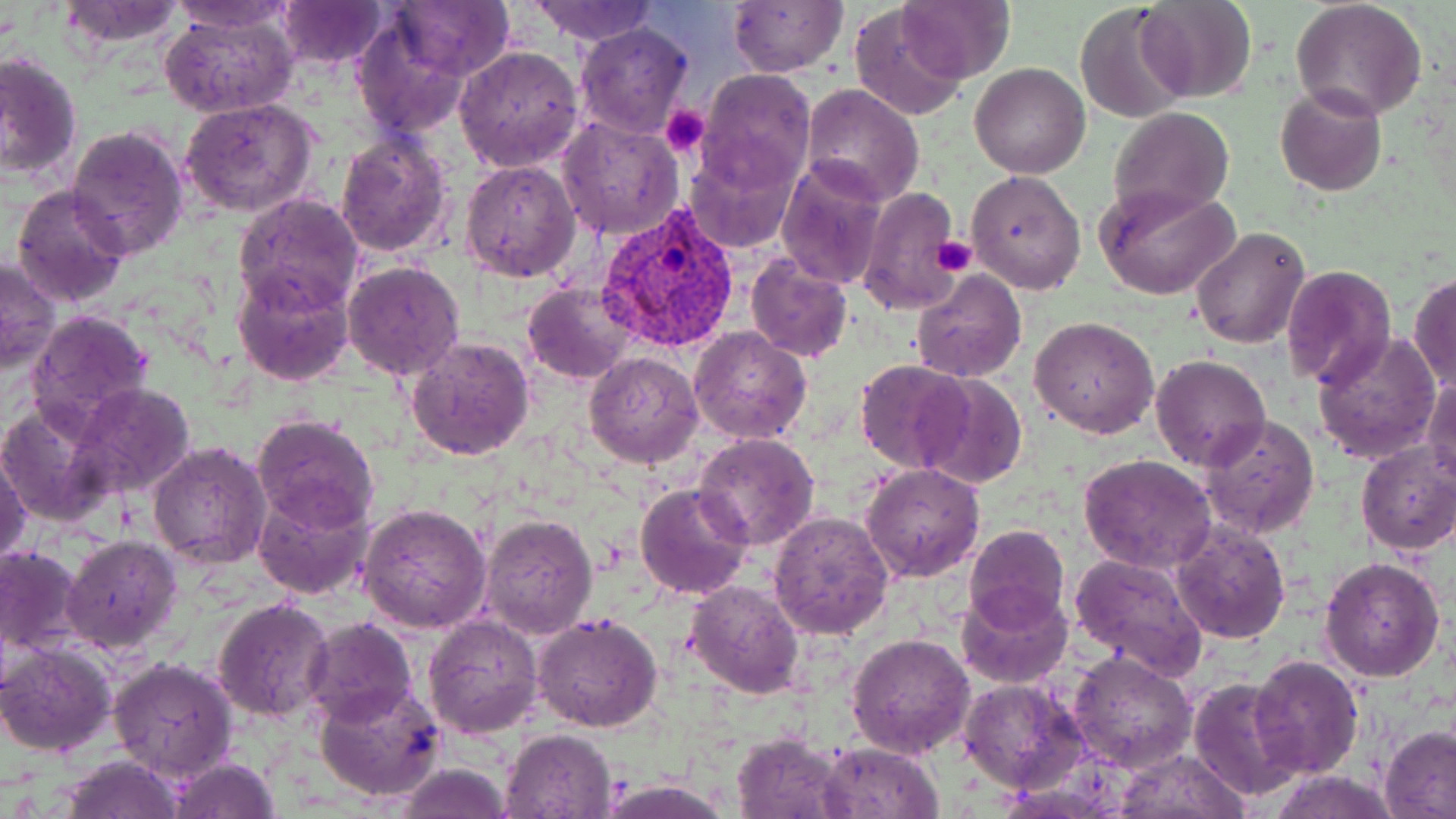

Approximate bounding boxes as (x1, y1, x2, y2) in pixels. Plasmodium vivax-infected red blood cell locations: (598, 202, 738, 356). Uninfected red blood cell locations: (171, 0, 297, 33), (277, 0, 388, 70), (285, 0, 509, 95), (390, 0, 512, 79), (899, 0, 1016, 83), (1135, 0, 1257, 102), (1291, 0, 1427, 120), (55, 1, 189, 50), (528, 1, 661, 47), (727, 1, 848, 76), (1073, 2, 1192, 123), (850, 8, 965, 122), (159, 10, 297, 117), (351, 14, 472, 137), (574, 23, 692, 138), (455, 45, 585, 172), (0, 51, 81, 180), (969, 63, 1091, 180), (696, 69, 815, 191), (801, 83, 924, 205), (1275, 85, 1388, 196), (180, 99, 318, 218), (1108, 106, 1234, 225), (557, 114, 684, 242), (66, 125, 189, 259), (335, 131, 453, 259), (683, 144, 798, 253), (776, 158, 887, 288), (461, 160, 580, 281), (966, 170, 1087, 295), (1094, 183, 1239, 300), (12, 184, 131, 308), (858, 185, 964, 314), (233, 193, 364, 315), (1191, 227, 1309, 349), (744, 256, 852, 363), (1, 258, 60, 375), (342, 261, 465, 381), (232, 263, 355, 386), (1281, 265, 1395, 389), (912, 266, 1027, 383), (1409, 272, 1456, 394), (523, 281, 638, 384), (25, 310, 157, 435), (1031, 315, 1159, 438), (690, 326, 813, 445), (1312, 329, 1442, 464), (405, 336, 535, 462), (584, 351, 704, 468), (1151, 355, 1271, 472), (855, 360, 972, 473), (914, 373, 1027, 491), (1424, 374, 1456, 490), (71, 383, 196, 499), (0, 404, 112, 528), (1200, 414, 1319, 538), (253, 415, 380, 532), (694, 433, 819, 550), (148, 442, 273, 569), (1356, 442, 1456, 554), (1, 450, 31, 565), (1080, 455, 1217, 572), (861, 464, 985, 583), (636, 481, 753, 599), (253, 485, 374, 601), (359, 502, 493, 633), (768, 511, 894, 641), (479, 514, 599, 639), (1172, 522, 1290, 643), (964, 524, 1069, 629), (61, 535, 183, 655), (0, 545, 87, 657), (1069, 551, 1207, 677), (1320, 556, 1446, 683), (684, 580, 805, 699), (955, 584, 1073, 689), (213, 596, 335, 720), (532, 612, 663, 733), (423, 614, 544, 738), (302, 617, 416, 730), (846, 633, 975, 759), (0, 641, 117, 758), (1068, 652, 1197, 774), (1249, 654, 1363, 778), (108, 657, 238, 783), (1068, 666, 1300, 793), (957, 676, 1089, 793), (1189, 676, 1307, 803), (315, 681, 445, 803), (1380, 724, 1456, 819), (502, 728, 618, 818), (732, 731, 854, 818), (818, 742, 944, 818), (1112, 747, 1249, 819), (57, 754, 187, 819), (168, 757, 281, 818), (389, 761, 517, 819), (1274, 771, 1398, 818), (601, 778, 731, 819). Platelet locations: (660, 106, 709, 157), (935, 237, 978, 277). Slide-level diagnosis: Plasmodium vivax. Image is 1456×819 pixels. May-Grünwald-Giemsa-stained preparation. Captured at 1000x magnification. Thin blood film. Single field of view. Light microscopy.